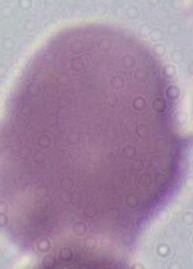
modality = micrograph
identification = red blood cell
magnification = 1000x